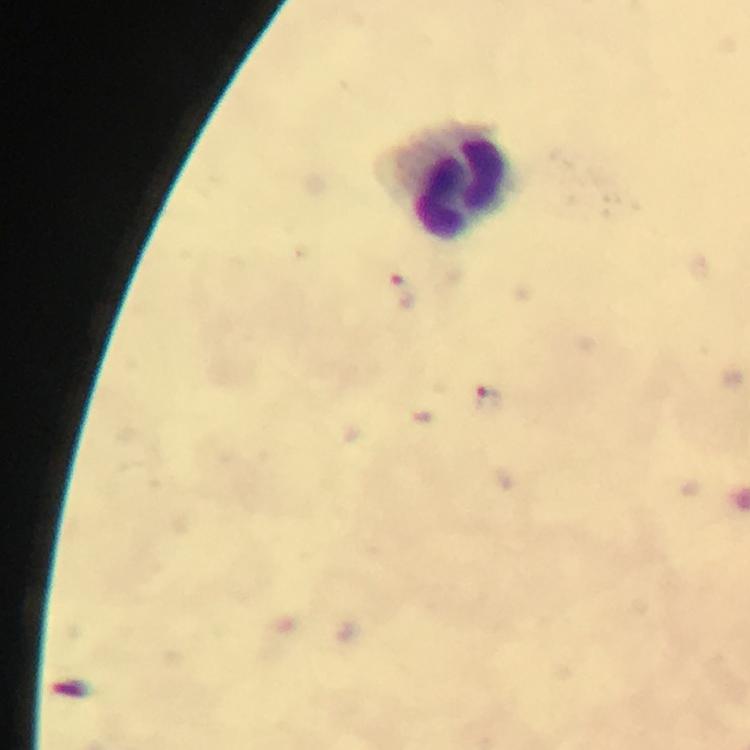

Approximate object centers, in pixels from the top-left corner. Malaria parasite locations: (x=405, y=293), (x=488, y=397). Leukocyte locations: (x=450, y=181). Thick blood smear. From a malaria diagnostic workup. Photographed with a smartphone mounted on the microscope. Cropped region of a single field of view. Immersion oil was used. At 100x magnification. Image is 750×750 pixels. Giemsa-stained preparation.